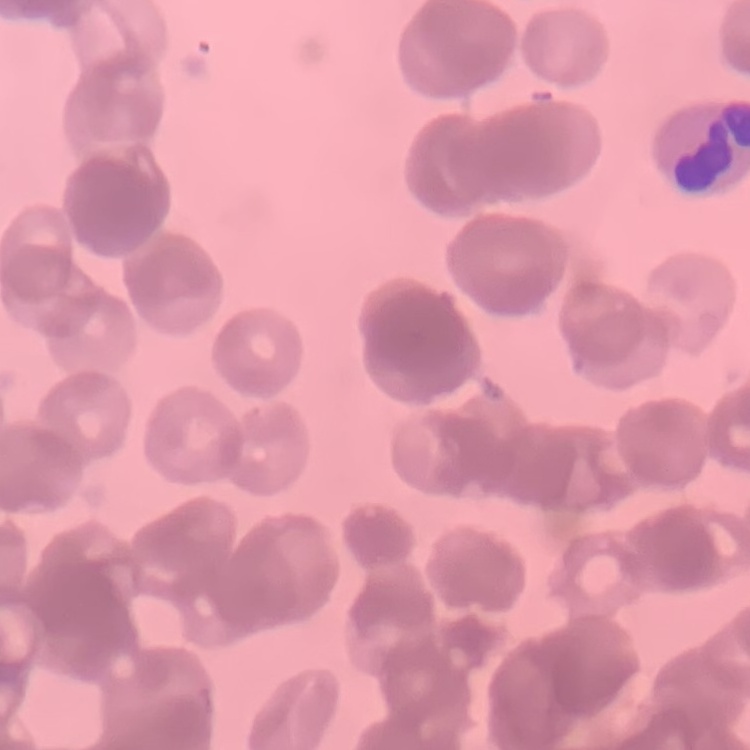 The erythrocytes show rouleaux formation. One tile cut from a larger photomicrograph. Thin blood smear. Stained with either Field's or Giemsa.